Point out each Plasmodium parasite.
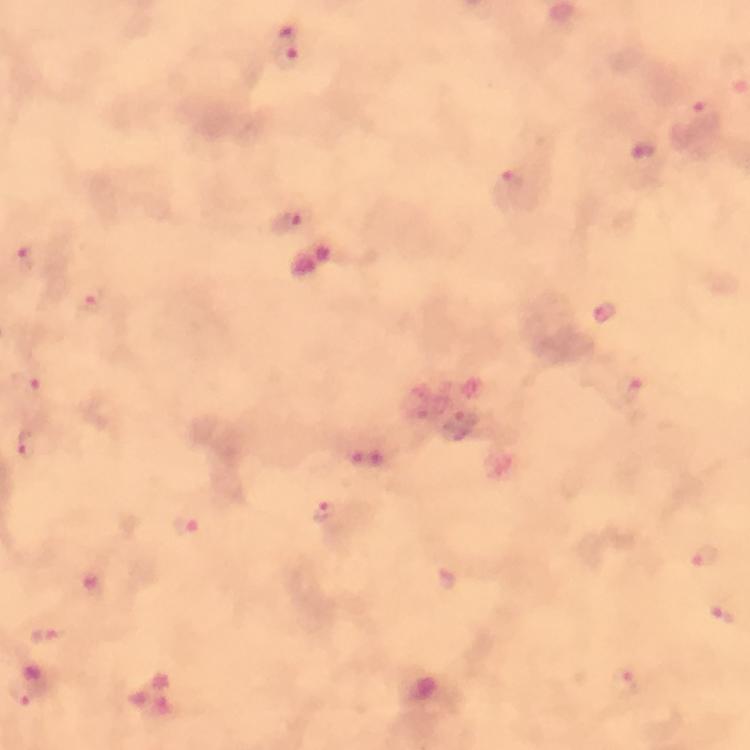
Approximate object centers, in pixels from the top-left corner.
Plasmodium parasites: (x=295, y=47), (x=702, y=117), (x=643, y=151), (x=510, y=187), (x=288, y=223), (x=26, y=259), (x=94, y=299), (x=606, y=310), (x=27, y=381), (x=630, y=389), (x=25, y=446), (x=373, y=462), (x=325, y=513), (x=186, y=527), (x=706, y=557), (x=97, y=587), (x=724, y=614), (x=45, y=637), (x=625, y=684), (x=28, y=689).

Image is 750×750 pixels. Photographed through the microscope with a smartphone camera. Giemsa-stained preparation. At 100x magnification. Cropped region of a single field of view. From a diagnostic examination for malaria. Immersion oil was used. Thick smear.